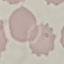

Result: no malaria parasites seen. Giemsa stain. Thin smear of blood. Acquired by smartphone through the microscope eyepiece. Cell patch, automatically extracted from a larger field of view and resized to 64 × 64 pixels.